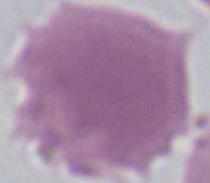

Captured at 1000x magnification. Photomicrograph. An erythrocyte is seen.